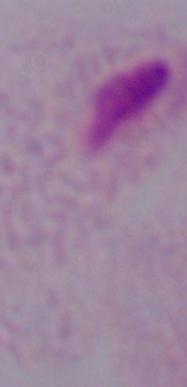

A trichomonad is seen. Captured at 1000x magnification. Photomicrograph.